Report the malaria status of this cell.
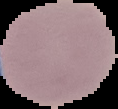

It is uninfected.

preparation = thin blood smear
image type = cell region segmented out of the field of view; surrounding area masked to black
image size = 118×109 pixels